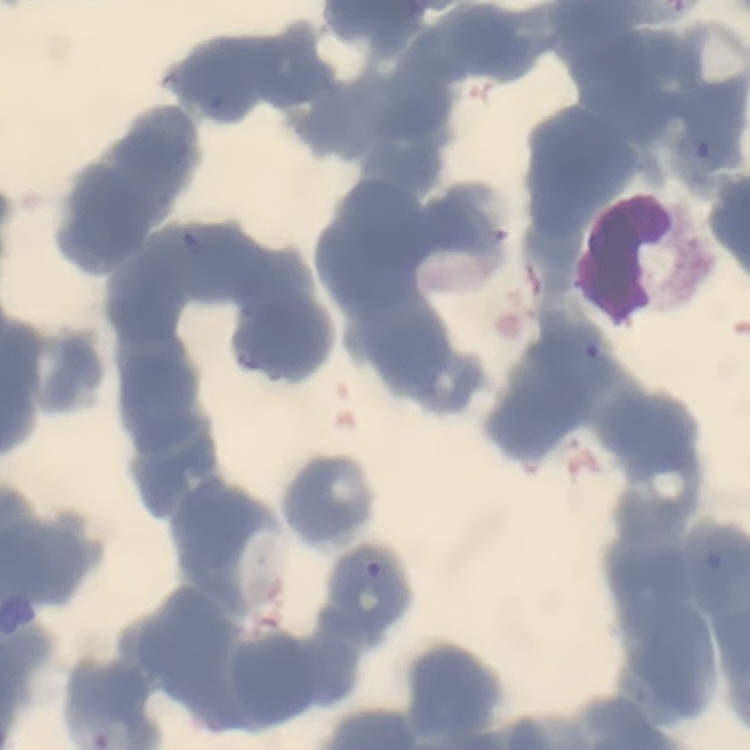
The red blood cells show rouleaux formation. Thin blood smear. Stained with either Field's or Giemsa. One tile cut from a larger photomicrograph.